Classify this cell by malaria status.
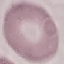

Uninfected.

capture = smartphone through the microscope eyepiece
stain = Giemsa
image type = cell patch, automatically extracted from a larger field of view and resized to 64 × 64 pixels
preparation = thin blood film